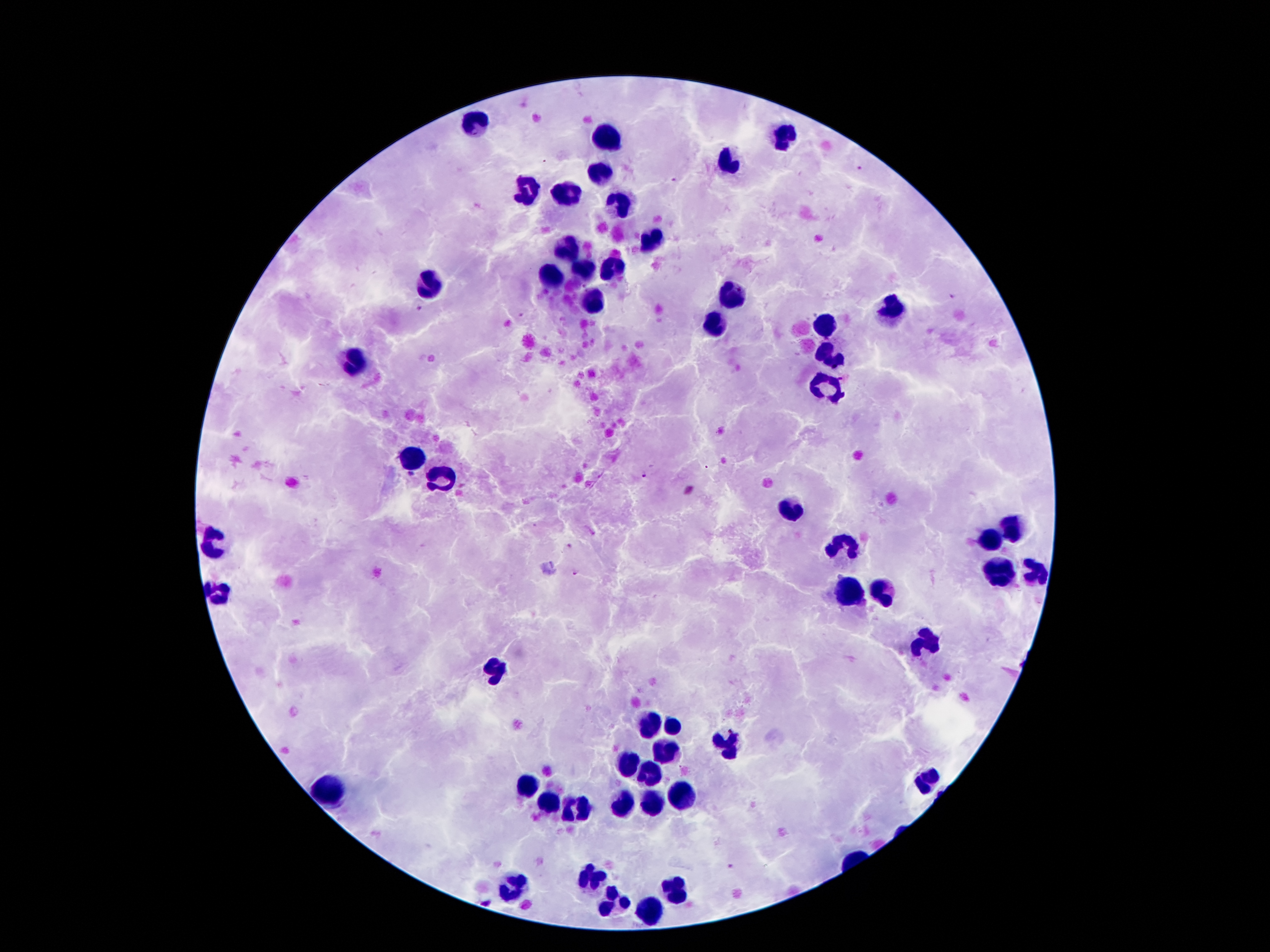
malaria_parasite_locations: 'approximate centers as (x, y) in pixels: (862, 169), (673, 180), (583, 287), (951, 296), (418, 307), (519, 316), (642, 474), (410, 476), (568, 544), (575, 572), (729, 867)'
patient_malaria_status: positive for Plasmodium falciparum
leukocyte_locations: 'approximate centers as (x, y) in pixels: (474, 122), (787, 131), (608, 138), (726, 161), (598, 175), (566, 191), (526, 192), (622, 205), (647, 240), (566, 248), (612, 268), (584, 269), (552, 278), (428, 283), (733, 295), (594, 301), (892, 312), (825, 327), (715, 328), (831, 356), (356, 362), (827, 382), (414, 461), (442, 479), (789, 508), (1016, 522), (215, 538), (988, 544), (841, 547), (999, 573), (1035, 573), (846, 591), (218, 593), (885, 593), (927, 643), (495, 668), (652, 723), (673, 727), (727, 747), (666, 749), (626, 764), (652, 775), (927, 780), (528, 788), (328, 790), (680, 798), (547, 805), (626, 805), (652, 805), (582, 808), (589, 880), (510, 885), (673, 893), (614, 901), (649, 911)'
magnification: 100x
image_size: 1270×952 pixels
capture: smartphone through the microscope eyepiece
stain: Giemsa
field_of_view: one from this slide
preparation: thick peripheral-blood smear